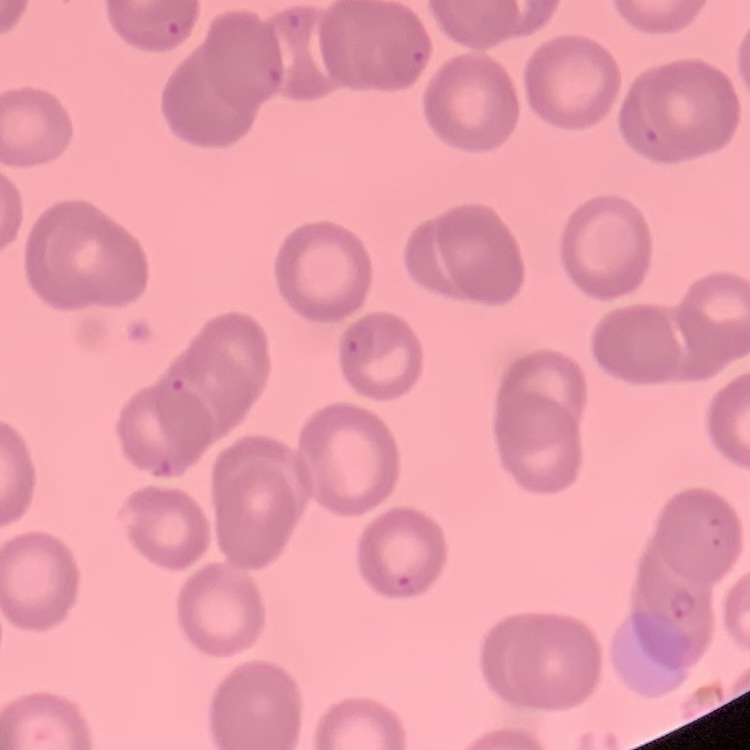
{
  "red_blood_cell_morphology": "no rouleaux formation",
  "image_type": "square crop of a larger photomicrograph",
  "preparation": "thin blood smear",
  "stain": "Field's or Giemsa"
}